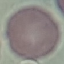
result: no malaria parasites detected
preparation: thin smear
capture: smartphone camera at the microscope eyepiece
image_type: automatically extracted cell patch, resized to 64 × 64 pixels
stain: Giemsa